Outline each blood parasite and name the species.
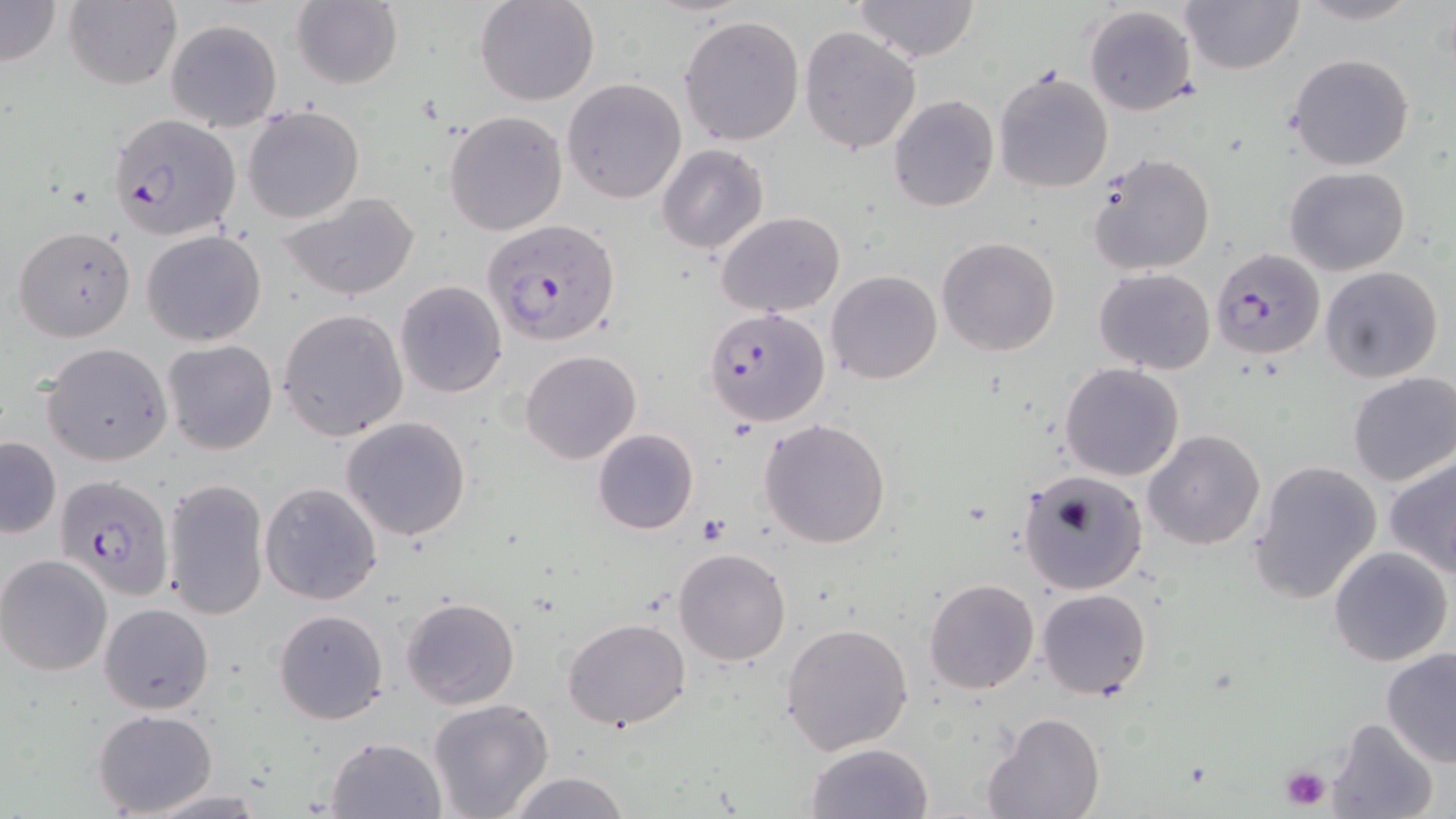

Approximate bounding boxes as (x1, y1, x2, y2) in pixels.
Plasmodium falciparum-infected red blood cells: (106, 110, 241, 241), (482, 218, 621, 346), (1209, 247, 1326, 361), (704, 306, 831, 426), (55, 473, 178, 602).
No Plasmodium ovale, Plasmodium malariae, Plasmodium vivax, Babesia divergens, or Trypanosoma brucei observed.

slide-level diagnosis = Plasmodium falciparum
preparation = thin blood smear
uninfected red blood cell locations = approximate bounding boxes as (x1, y1, x2, y2) in pixels: (0, 0, 62, 68), (473, 0, 601, 106), (852, 0, 982, 65), (1295, 0, 1423, 25), (63, 1, 181, 89), (290, 1, 403, 89), (1181, 1, 1304, 75), (1082, 4, 1198, 117), (678, 14, 805, 146), (166, 18, 282, 130), (799, 25, 922, 155), (1288, 54, 1415, 172), (994, 70, 1114, 194), (561, 78, 687, 205), (888, 95, 998, 213), (242, 104, 365, 224), (443, 109, 568, 236), (657, 143, 770, 255), (1086, 151, 1218, 277), (1284, 167, 1410, 277), (282, 194, 420, 300), (716, 211, 846, 317), (13, 225, 136, 342), (141, 230, 267, 346), (935, 237, 1061, 357), (1320, 265, 1442, 383), (1094, 268, 1217, 375), (826, 269, 942, 385), (395, 280, 507, 398), (278, 308, 408, 440), (163, 339, 278, 456), (40, 342, 172, 466), (519, 350, 641, 464), (1060, 364, 1184, 480), (1347, 372, 1456, 487), (341, 415, 473, 541), (758, 418, 892, 548), (591, 428, 698, 535), (1143, 429, 1266, 550), (0, 437, 61, 539), (1383, 453, 1456, 578), (1247, 459, 1383, 605), (1016, 469, 1148, 594), (163, 477, 269, 621), (260, 482, 383, 605), (1328, 546, 1453, 666), (674, 548, 791, 665), (0, 554, 114, 676), (923, 577, 1039, 695), (1036, 587, 1152, 699), (400, 597, 521, 711), (98, 602, 214, 714), (273, 608, 389, 724), (562, 617, 692, 732), (781, 623, 914, 754), (1379, 648, 1456, 768), (428, 699, 555, 819), (91, 707, 218, 815), (983, 713, 1106, 819), (1324, 717, 1438, 819), (325, 735, 445, 818), (804, 742, 935, 819), (504, 771, 632, 818), (146, 790, 268, 818)
modality = light microscopy
magnification = 1000x
image size = 1456×819 pixels
stain = May-Grünwald-Giemsa
field of view = one of a larger specimen
platelet locations = approximate bounding boxes as (x1, y1, x2, y2) in pixels: (699, 517, 730, 545), (1279, 764, 1333, 810)